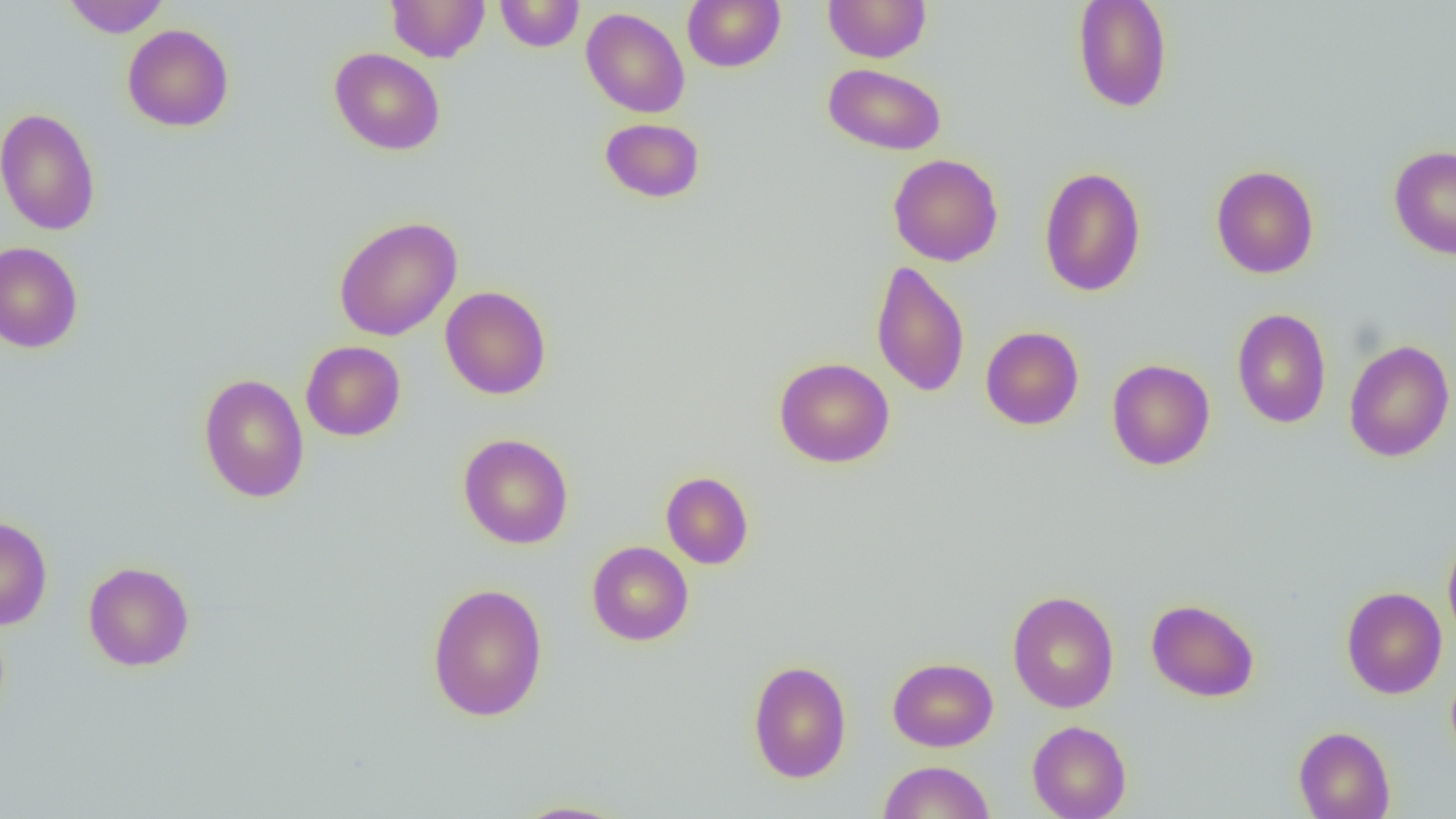

slide-level diagnosis = negative for blood parasites
image size = 1456×819 pixels
modality = light microscopy
magnification = 1000x
field of view = single
uninfected red blood cell locations = approximate bounding boxes as (x1, y1, x2, y2) in pixels: (63, 0, 170, 37), (386, 0, 489, 62), (495, 0, 584, 52), (683, 0, 785, 72), (823, 0, 931, 62), (1072, 0, 1173, 113), (581, 7, 690, 118), (122, 24, 234, 132), (329, 47, 446, 155), (823, 63, 947, 155), (0, 107, 101, 236), (599, 117, 705, 203), (1388, 145, 1456, 260), (888, 154, 1004, 266), (1211, 164, 1319, 279), (1039, 166, 1146, 296), (333, 216, 462, 341), (0, 242, 84, 353), (870, 260, 971, 397), (440, 285, 552, 399), (1232, 308, 1332, 428), (980, 326, 1084, 430), (1343, 339, 1455, 462), (300, 341, 406, 441), (774, 357, 894, 468), (1106, 359, 1215, 470), (199, 373, 309, 503), (458, 432, 574, 549), (660, 471, 754, 569), (0, 516, 52, 630), (1443, 532, 1456, 645), (587, 541, 693, 646), (83, 561, 194, 671), (427, 582, 548, 722), (1341, 586, 1447, 699), (1007, 590, 1120, 713), (1146, 598, 1259, 702), (887, 657, 998, 752), (748, 659, 852, 783), (1027, 720, 1131, 819), (1294, 726, 1395, 819), (877, 760, 995, 819), (509, 799, 632, 818)
preparation = thin blood film